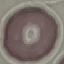
result = no malaria parasites detected
preparation = thin blood film
stain = Giemsa
image type = automatically extracted cell patch, resized to 64 × 64 pixels
capture = smartphone camera at the microscope eyepiece